Assess this cell for malaria.
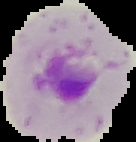
It is parasitized.

{
  "preparation": "thin blood smear",
  "image_type": "segmented cell region with the area outside set to black",
  "image_size": "136×142 pixels"
}